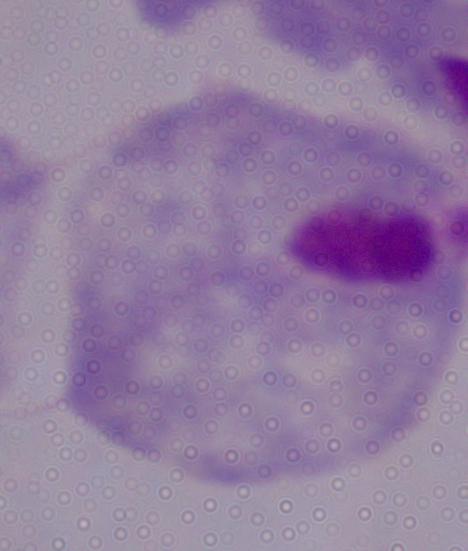

A trichomonad is seen. Photomicrograph. Captured at 1000x magnification.